Report the malaria status of this cell.
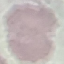

Uninfected.

Acquired by smartphone through the microscope eyepiece. Cell patch, automatically extracted from a larger field of view and resized to 64 × 64 pixels. Thin smear of blood. Giemsa-stained preparation.